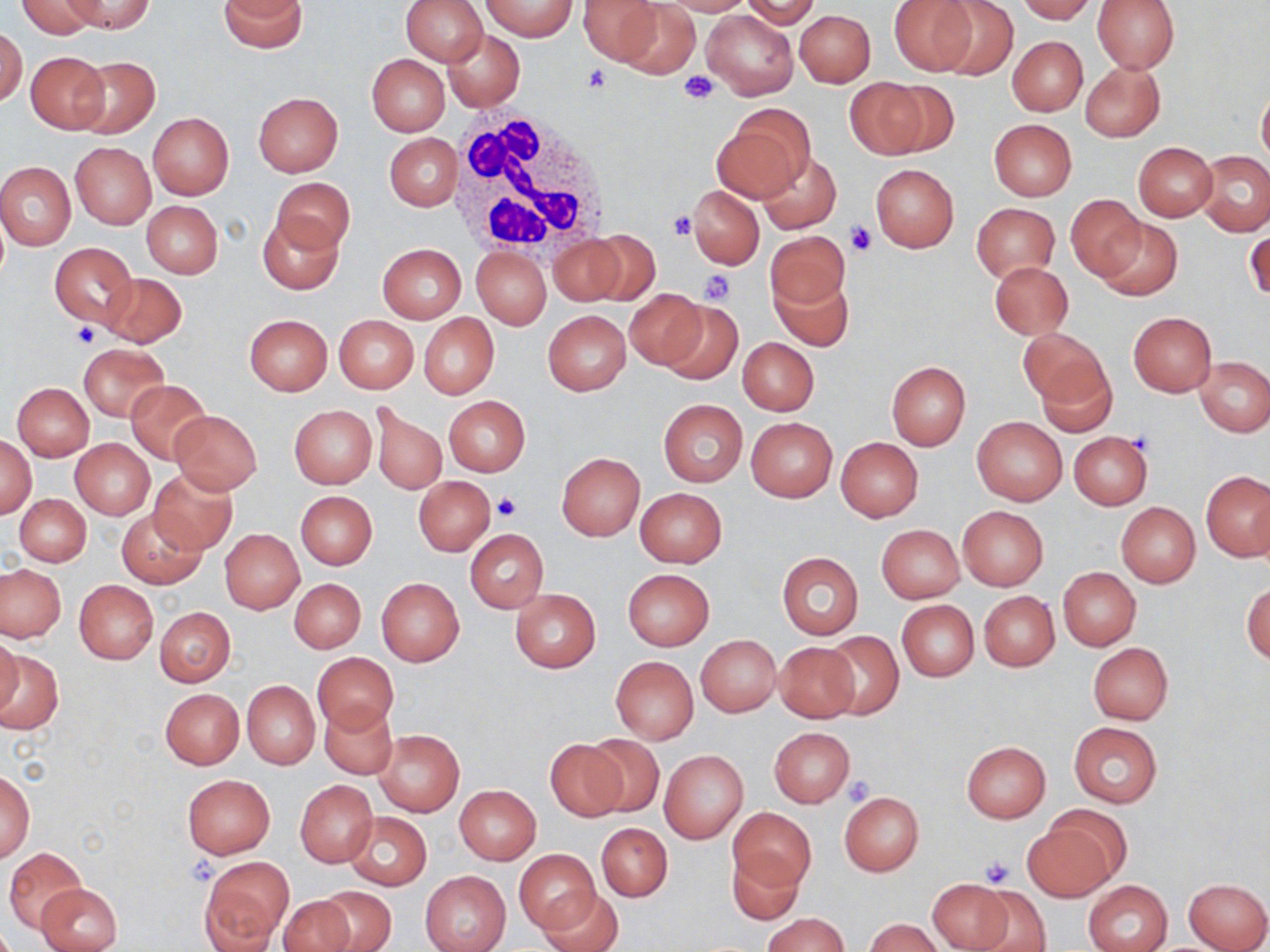
Approximate bounding boxes as (x1, y1, x2, y2) in pixels. White blood cell locations: (446, 107, 614, 258). Platelet locations: (582, 64, 612, 94), (680, 71, 719, 105), (667, 209, 696, 240), (845, 220, 875, 257), (699, 269, 736, 305), (71, 323, 100, 349), (492, 489, 521, 520), (843, 777, 876, 806), (980, 856, 1016, 888). Uninfected red blood cell locations: (16, 0, 100, 39), (61, 0, 154, 34), (401, 0, 486, 65), (482, 0, 576, 40), (578, 0, 664, 65), (658, 0, 753, 15), (741, 0, 821, 27), (890, 0, 979, 73), (931, 0, 1019, 81), (1016, 0, 1095, 23), (1092, 0, 1180, 73), (218, 1, 307, 53), (616, 1, 700, 79), (702, 9, 797, 99), (795, 9, 875, 87), (0, 27, 27, 108), (442, 29, 525, 110), (1008, 37, 1087, 115), (26, 52, 109, 133), (367, 54, 449, 136), (69, 55, 160, 138), (1081, 61, 1165, 141), (846, 77, 933, 159), (1258, 84, 1270, 169), (253, 92, 343, 177), (713, 107, 814, 201), (148, 113, 234, 199), (989, 118, 1077, 199), (385, 133, 461, 211), (71, 142, 156, 228), (1133, 142, 1218, 221), (757, 151, 841, 232), (1196, 151, 1270, 235), (0, 162, 76, 251), (871, 164, 958, 252), (272, 177, 354, 254), (690, 185, 763, 269), (1066, 194, 1144, 279), (142, 201, 224, 279), (972, 203, 1059, 283), (257, 212, 342, 294), (1095, 218, 1182, 300), (1245, 227, 1269, 305), (765, 230, 850, 314), (588, 232, 659, 305), (549, 235, 626, 307), (50, 243, 137, 327), (377, 244, 466, 323), (472, 246, 551, 330), (989, 261, 1073, 340), (770, 268, 854, 350), (101, 273, 187, 348), (626, 289, 707, 368), (658, 302, 742, 385), (543, 310, 631, 394), (1129, 312, 1217, 396), (418, 313, 499, 398), (244, 314, 332, 394), (335, 315, 419, 393), (1020, 328, 1113, 419), (737, 337, 819, 415), (79, 344, 168, 420), (1196, 357, 1270, 437), (886, 361, 970, 451), (125, 380, 211, 464), (11, 382, 94, 461), (443, 395, 530, 476), (659, 400, 747, 486), (372, 404, 447, 496), (289, 405, 377, 487), (169, 410, 263, 496), (972, 417, 1066, 505), (747, 418, 836, 502), (1068, 431, 1152, 510), (1, 436, 36, 517), (836, 437, 923, 521), (70, 439, 154, 518), (557, 453, 644, 541), (148, 468, 237, 554), (1202, 469, 1269, 561), (414, 476, 497, 556), (634, 488, 728, 567), (296, 491, 378, 569), (14, 494, 90, 566), (1116, 502, 1201, 588), (957, 506, 1048, 590), (116, 507, 205, 589), (876, 524, 965, 604), (220, 529, 304, 612), (464, 529, 549, 613), (777, 552, 864, 639), (1, 564, 65, 641), (1058, 567, 1141, 650), (623, 568, 715, 652), (377, 577, 464, 666), (290, 578, 366, 654), (74, 579, 158, 664), (1242, 583, 1270, 665), (510, 588, 601, 672), (980, 591, 1058, 671), (896, 600, 979, 681), (155, 607, 235, 686), (822, 630, 903, 720), (695, 634, 782, 716), (1, 635, 23, 720), (774, 643, 860, 722), (1089, 643, 1173, 724), (0, 648, 64, 736), (312, 652, 398, 735), (611, 656, 698, 743), (242, 680, 319, 769), (161, 688, 243, 768), (320, 702, 397, 779), (1067, 722, 1162, 809), (769, 726, 855, 807), (373, 729, 464, 817), (585, 733, 663, 816), (545, 740, 629, 820), (960, 741, 1051, 823), (659, 749, 747, 844), (1, 769, 35, 863), (181, 774, 275, 857), (296, 780, 378, 866), (455, 785, 541, 863), (839, 791, 924, 875), (729, 807, 815, 890), (344, 812, 432, 891), (1021, 820, 1117, 901), (597, 823, 672, 901), (4, 847, 86, 932), (515, 848, 602, 934), (729, 848, 805, 926), (200, 858, 292, 947), (420, 870, 511, 952), (925, 878, 1015, 952), (1184, 878, 1269, 952), (1085, 879, 1173, 952), (36, 882, 122, 952), (969, 885, 1053, 952), (315, 886, 396, 952), (539, 888, 623, 952), (277, 895, 356, 952), (764, 913, 847, 952), (866, 918, 942, 952). Slide-level diagnosis: no evidence of blood parasites. Image is 1270×952 pixels. One field of a larger specimen. Thin blood smear. Captured at 1000x magnification. Light microscopy. May-Grünwald-Giemsa stain.